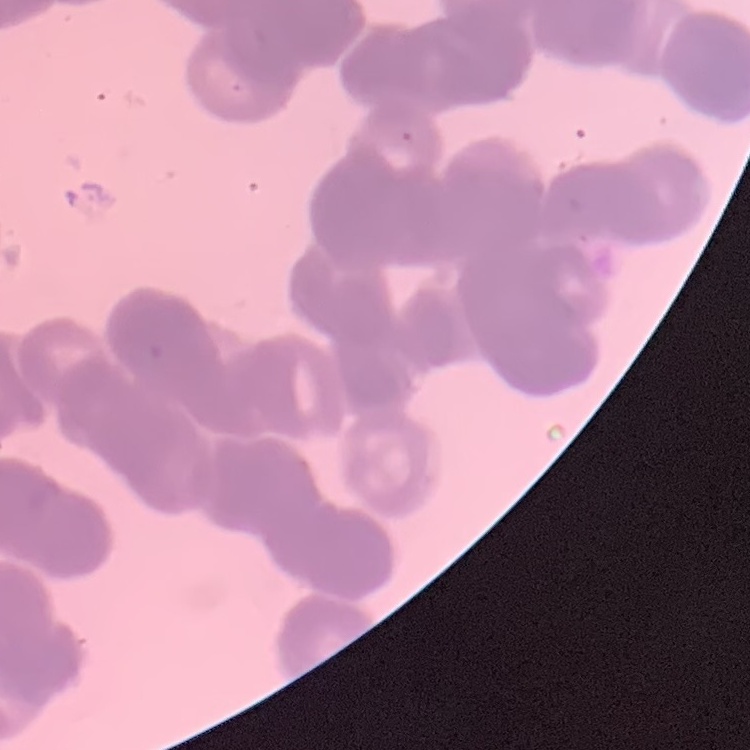 The red blood cells exhibit rouleaux formation. Field's or Giemsa stain. One tile cut from a larger photomicrograph. Thin peripheral smear.